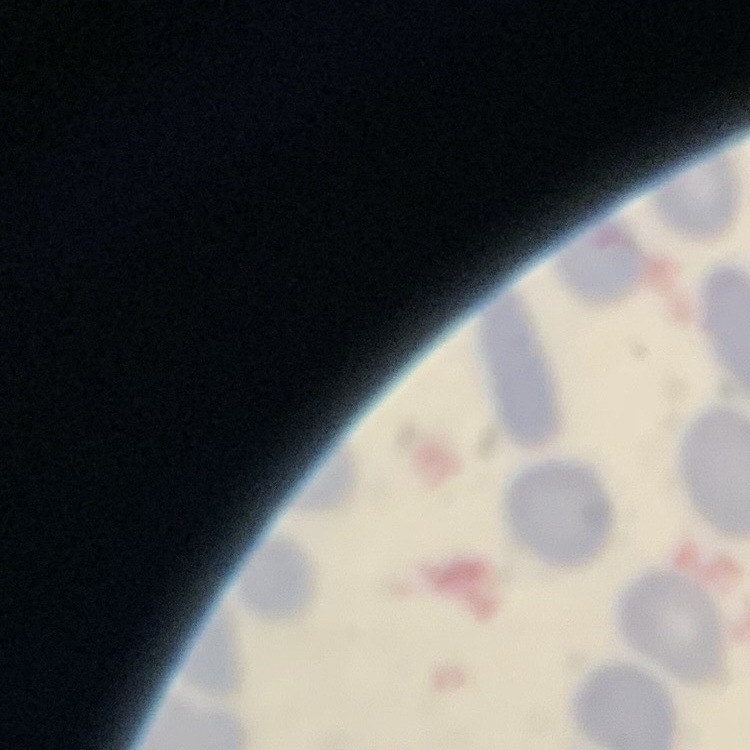

The red blood cells show no rouleaux formation. Square crop of a larger photomicrograph. Thin blood smear. Field's or Giemsa stain.